Outline each blood parasite and name the species.
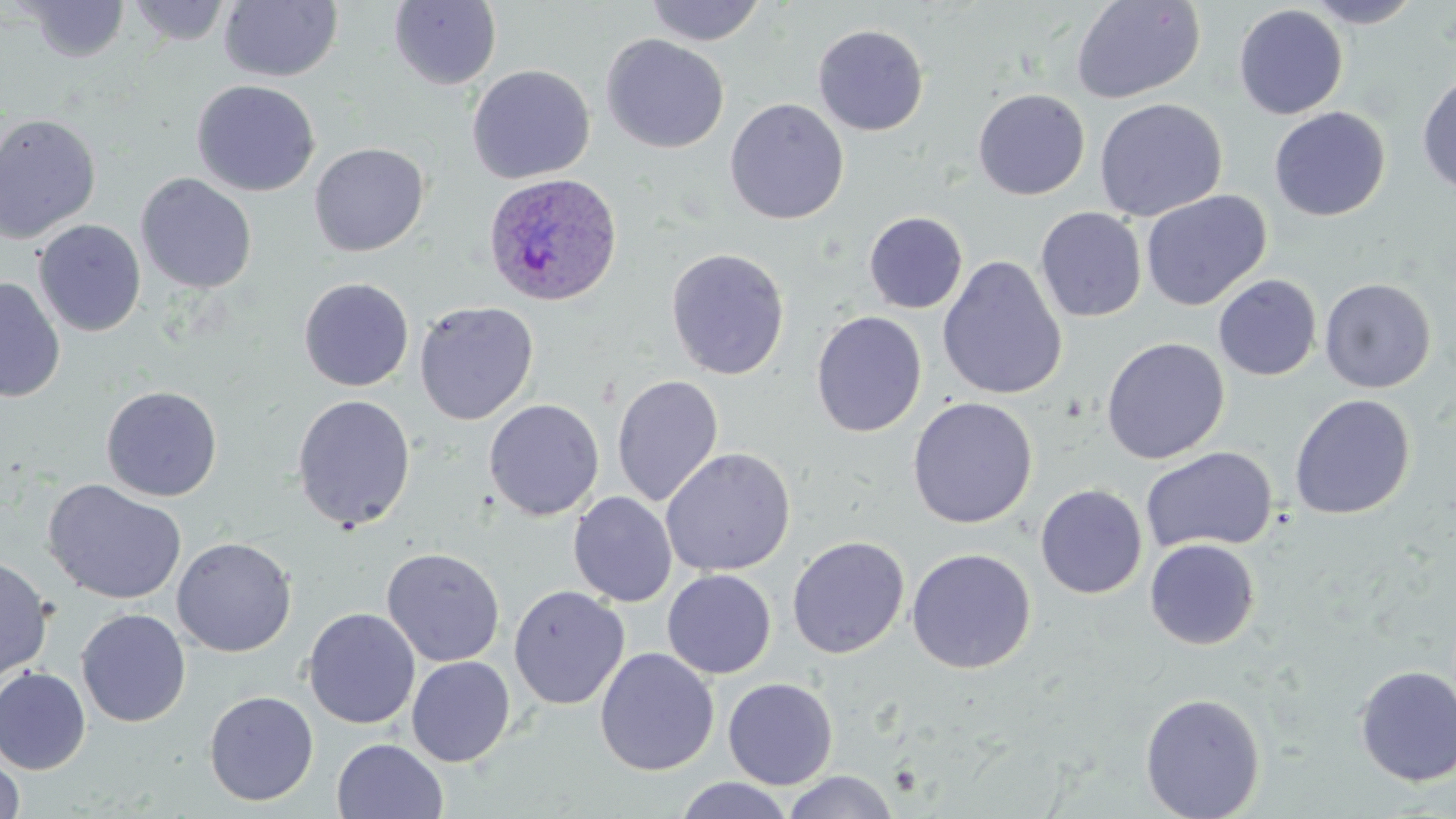

Approximate bounding boxes as named x1/y1/x2/y2 corners in pixels.
Plasmodium ovale-infected red blood cells: (x1=482, y1=172, x2=623, y2=307).
No Plasmodium falciparum, Plasmodium malariae, Plasmodium vivax, Babesia divergens, or Trypanosoma brucei observed.

Summary:
  - Uninfected red blood cell locations: (x1=19, y1=0, x2=131, y2=63), (x1=1070, y1=0, x2=1206, y2=104), (x1=1305, y1=0, x2=1424, y2=28), (x1=127, y1=1, x2=233, y2=45), (x1=219, y1=1, x2=343, y2=83), (x1=388, y1=1, x2=502, y2=90), (x1=644, y1=1, x2=767, y2=46), (x1=1233, y1=4, x2=1348, y2=119), (x1=812, y1=23, x2=929, y2=136), (x1=601, y1=34, x2=729, y2=153), (x1=466, y1=64, x2=594, y2=184), (x1=1417, y1=71, x2=1456, y2=198), (x1=191, y1=80, x2=320, y2=197), (x1=972, y1=89, x2=1090, y2=200), (x1=1094, y1=97, x2=1228, y2=222), (x1=725, y1=98, x2=849, y2=225), (x1=1269, y1=107, x2=1391, y2=221), (x1=0, y1=113, x2=102, y2=244), (x1=309, y1=142, x2=430, y2=256), (x1=136, y1=173, x2=257, y2=294), (x1=1140, y1=190, x2=1271, y2=310), (x1=1035, y1=206, x2=1147, y2=322), (x1=863, y1=211, x2=968, y2=314), (x1=33, y1=219, x2=146, y2=337), (x1=665, y1=248, x2=790, y2=380), (x1=937, y1=254, x2=1068, y2=401), (x1=1213, y1=274, x2=1322, y2=381), (x1=0, y1=277, x2=65, y2=403), (x1=299, y1=277, x2=414, y2=391), (x1=1319, y1=278, x2=1436, y2=393), (x1=414, y1=300, x2=539, y2=425), (x1=811, y1=311, x2=927, y2=438), (x1=1101, y1=336, x2=1230, y2=464), (x1=611, y1=374, x2=724, y2=508), (x1=101, y1=385, x2=223, y2=502), (x1=291, y1=394, x2=416, y2=531), (x1=1289, y1=394, x2=1415, y2=520), (x1=907, y1=396, x2=1038, y2=529), (x1=484, y1=398, x2=605, y2=521), (x1=1141, y1=446, x2=1278, y2=554), (x1=660, y1=447, x2=796, y2=577), (x1=42, y1=479, x2=187, y2=605), (x1=1035, y1=485, x2=1147, y2=598), (x1=568, y1=492, x2=677, y2=607), (x1=787, y1=535, x2=909, y2=658), (x1=171, y1=536, x2=297, y2=657), (x1=1144, y1=539, x2=1260, y2=650), (x1=382, y1=547, x2=505, y2=667), (x1=906, y1=548, x2=1036, y2=674), (x1=0, y1=556, x2=53, y2=682), (x1=662, y1=569, x2=776, y2=679), (x1=508, y1=585, x2=630, y2=710), (x1=303, y1=607, x2=421, y2=729), (x1=76, y1=608, x2=191, y2=727), (x1=594, y1=647, x2=719, y2=776), (x1=406, y1=656, x2=515, y2=767), (x1=1353, y1=665, x2=1456, y2=787), (x1=1, y1=666, x2=91, y2=775), (x1=723, y1=677, x2=838, y2=789), (x1=204, y1=690, x2=319, y2=806), (x1=1139, y1=693, x2=1266, y2=818), (x1=332, y1=739, x2=448, y2=819), (x1=0, y1=747, x2=25, y2=819), (x1=782, y1=770, x2=898, y2=819), (x1=673, y1=776, x2=795, y2=818)
  - Slide-level diagnosis: Plasmodium ovale
  - Modality: optical microscopy
  - Magnification: 1000x
  - Field of view: one of a larger specimen
  - Preparation: thin blood film
  - Image size: 1456×819 pixels
  - Stain: May-Grünwald-Giemsa